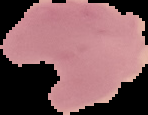
Malaria status: parasitized. From a thin blood smear. Image is 148×115 pixels. Cell region segmented out of the field of view; the surrounding area is masked to black.